Name the cell type shown.
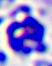
This is a leukocyte.

Micrograph. Captured at 400x magnification.